Outline each uninfected red blood cell.
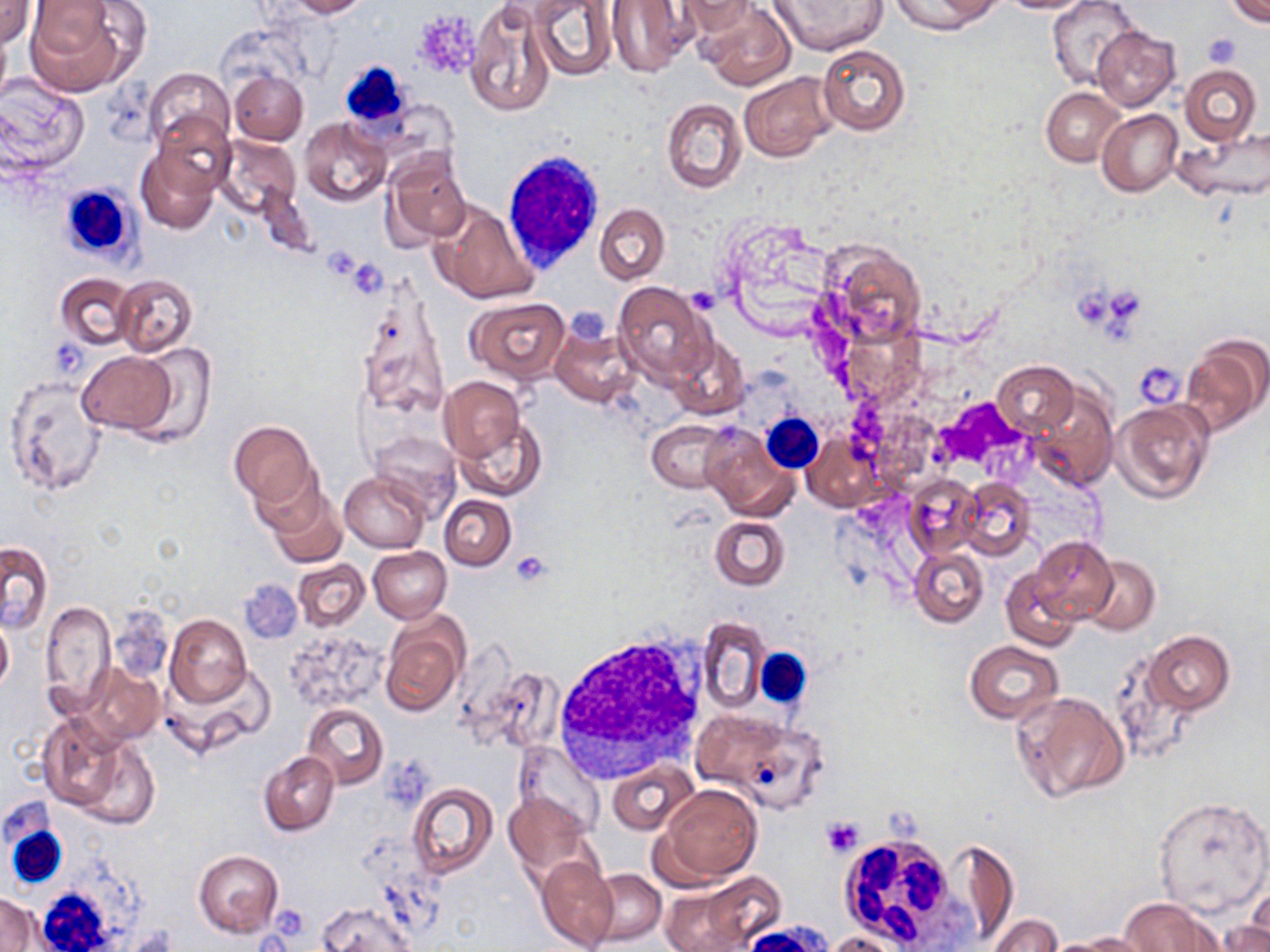

Approximate bounding boxes as (x1, y1, x2, y2) in pixels.
Uninfected red blood cells: (28, 0, 143, 95), (283, 0, 368, 18), (464, 0, 558, 117), (677, 0, 761, 40), (889, 0, 999, 34), (995, 0, 1102, 14), (1048, 0, 1139, 89), (1226, 0, 1270, 27), (1, 1, 37, 47), (528, 1, 616, 81), (607, 1, 696, 75), (769, 1, 886, 55), (696, 3, 795, 89), (1092, 25, 1180, 112), (0, 30, 11, 104), (817, 45, 910, 135), (1179, 64, 1261, 146), (145, 67, 233, 151), (229, 71, 308, 145), (738, 71, 839, 162), (0, 76, 89, 175), (1041, 87, 1124, 166), (660, 98, 746, 194), (1097, 109, 1182, 198), (155, 113, 234, 196), (300, 117, 391, 207), (1177, 127, 1270, 201), (216, 135, 301, 220), (137, 143, 222, 234), (384, 153, 471, 247), (429, 201, 540, 305), (594, 203, 668, 284), (717, 215, 840, 335), (816, 239, 926, 346), (55, 273, 136, 350), (113, 274, 198, 358), (353, 279, 450, 427), (613, 281, 714, 385), (466, 296, 570, 384), (551, 323, 638, 407), (669, 335, 748, 419), (1181, 336, 1269, 435), (128, 343, 216, 446), (77, 351, 176, 435), (992, 361, 1078, 437), (4, 375, 109, 496), (438, 376, 524, 465), (1027, 382, 1118, 491), (1111, 398, 1215, 504), (452, 414, 545, 502), (229, 420, 319, 506), (648, 420, 731, 492), (699, 423, 799, 521), (365, 430, 462, 518), (803, 434, 880, 512), (254, 471, 336, 547), (340, 471, 429, 553), (904, 474, 983, 559), (957, 477, 1036, 562), (267, 491, 347, 569), (440, 494, 515, 570), (710, 516, 790, 590), (1030, 537, 1118, 622), (1, 540, 54, 634), (908, 546, 988, 627), (367, 547, 450, 623), (1079, 555, 1160, 636), (292, 559, 369, 631), (1001, 569, 1080, 651), (41, 600, 115, 713), (166, 615, 252, 707), (380, 615, 469, 717), (697, 616, 769, 713), (0, 618, 13, 693), (288, 629, 386, 710), (1144, 630, 1234, 716), (964, 640, 1062, 724), (82, 663, 165, 745), (470, 664, 565, 754), (167, 665, 275, 756), (1013, 689, 1127, 805), (301, 703, 389, 790), (690, 706, 812, 799), (38, 711, 140, 816), (71, 733, 161, 828), (514, 740, 604, 835), (260, 752, 340, 835), (608, 761, 698, 835), (655, 782, 761, 885), (407, 783, 500, 878), (502, 791, 595, 881), (1153, 797, 1269, 915), (955, 842, 1019, 941), (193, 849, 284, 937), (537, 856, 618, 952), (587, 869, 666, 946), (659, 880, 772, 951), (1246, 884, 1269, 948), (0, 892, 39, 952), (1118, 897, 1220, 951), (318, 902, 413, 952), (987, 914, 1063, 952), (1224, 914, 1270, 952), (822, 930, 912, 952), (1074, 932, 1158, 951), (1039, 937, 1134, 951).

White blood cell locations: (339, 61, 412, 131), (503, 146, 608, 276), (58, 181, 140, 263), (759, 412, 824, 474), (556, 632, 708, 778), (753, 647, 811, 712), (2, 791, 77, 888), (836, 830, 966, 950), (33, 884, 122, 951). Platelet locations: (412, 8, 482, 82), (1202, 32, 1244, 69), (346, 260, 389, 296), (1068, 283, 1111, 332), (687, 285, 720, 315), (1112, 286, 1139, 324), (565, 305, 616, 345), (52, 339, 90, 377), (1134, 360, 1186, 408), (933, 396, 1030, 474), (510, 551, 552, 588), (238, 578, 302, 644), (106, 604, 173, 684), (382, 756, 430, 811), (821, 816, 864, 858), (275, 907, 301, 939). Slide-level diagnosis: no evidence of blood parasites. One field of a larger specimen. Image is 1270×952 pixels. Thin blood smear. Light microscopy. May-Grünwald-Giemsa stain. 1000x magnification.